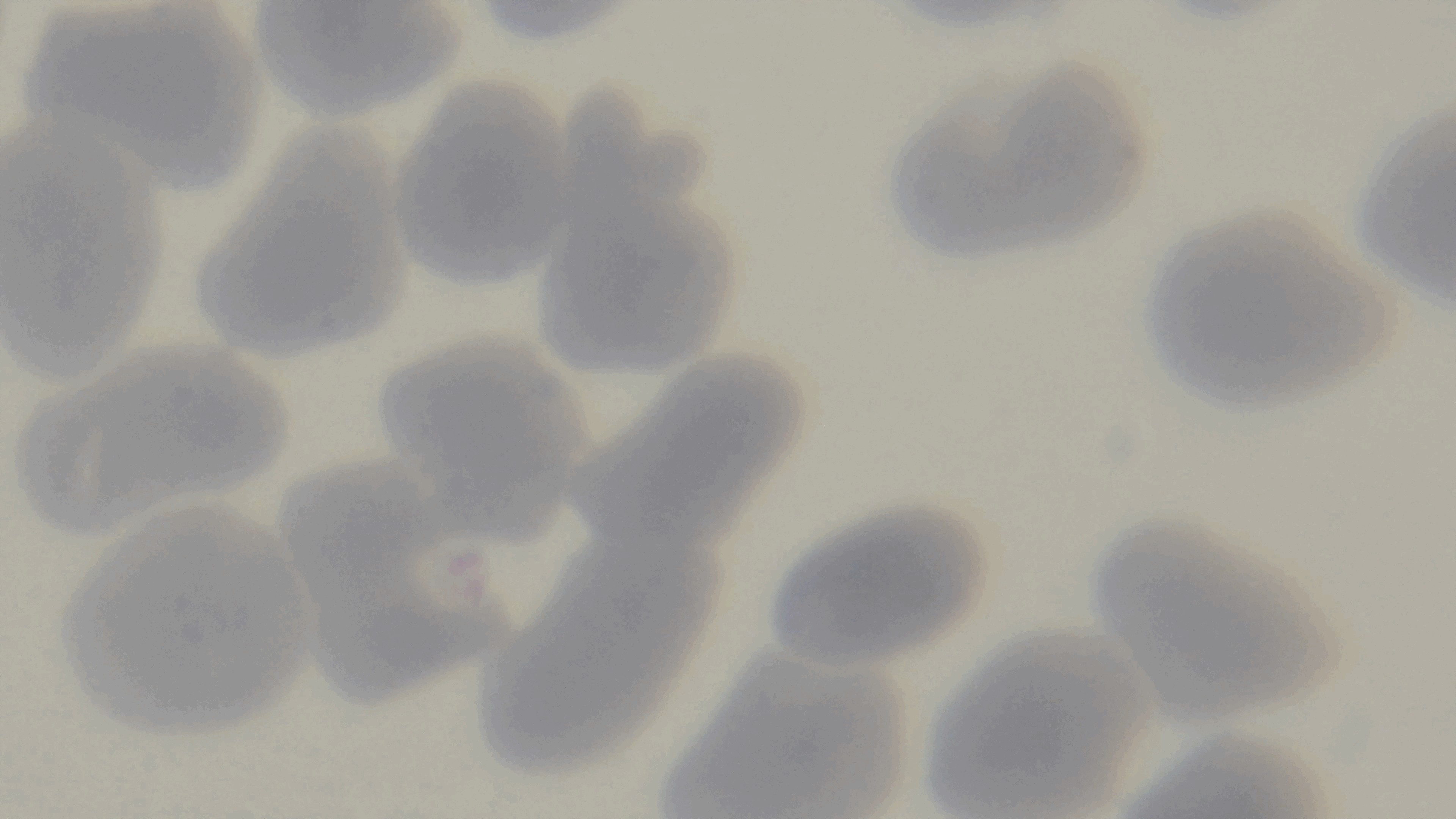

modality = light microscopy
stain = Giemsa
preparation = thin blood film
field of view = single
malaria status = uninfected
capture = mounted 4K digital camera
objective = 100x oil immersion